Outline each blood parasite and name the species.
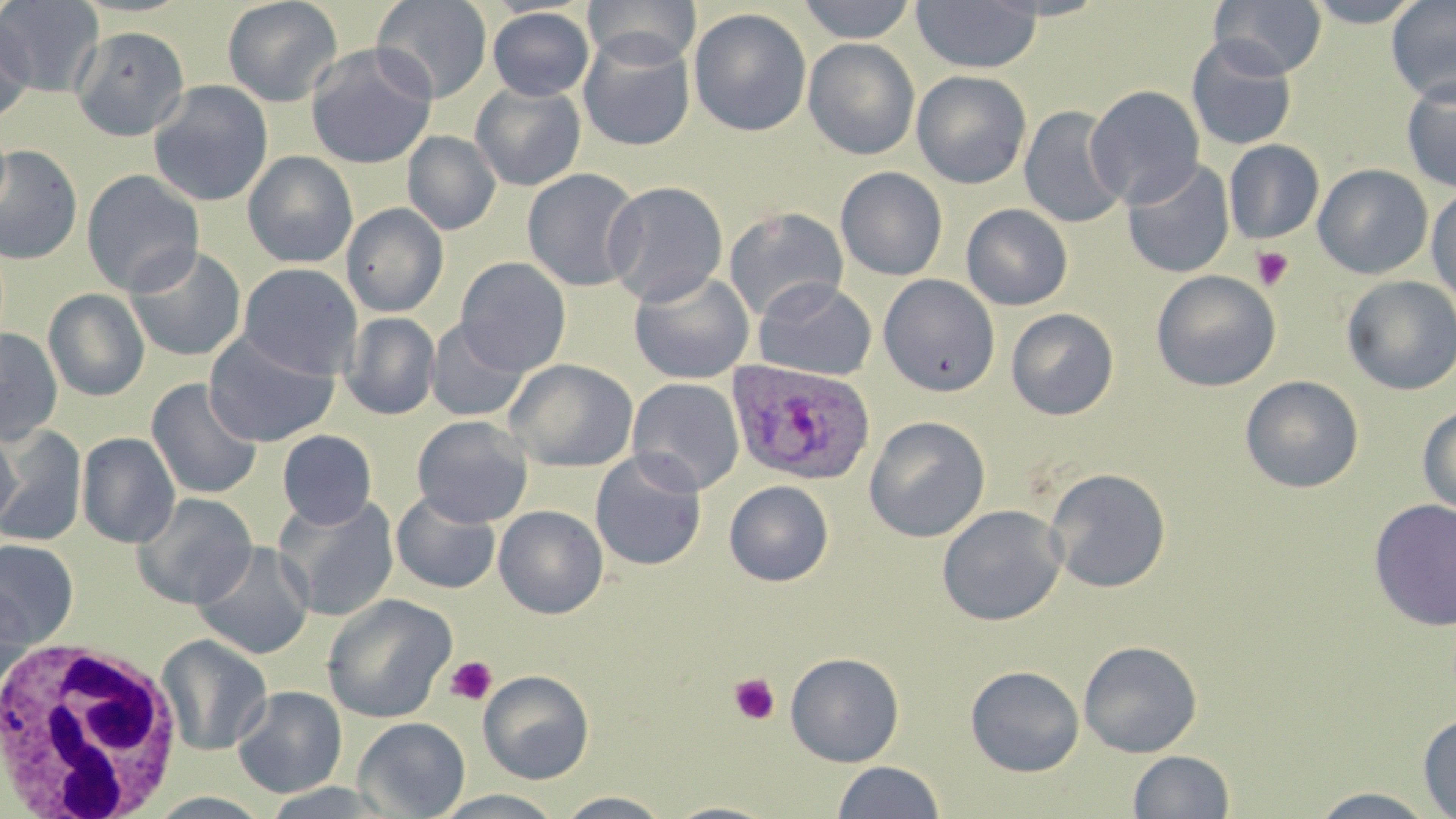

Approximate bounding boxes as [x1, y1, x2, y2] in pixels.
Plasmodium ovale-infected red blood cells: [726, 358, 876, 486].
No Plasmodium falciparum, Plasmodium malariae, Plasmodium vivax, Babesia divergens, or Trypanosoma brucei observed.

{
  "slide_level_diagnosis": "Plasmodium ovale",
  "platelet_locations": "approximate bounding boxes as [x1, y1, x2, y2] in pixels: [1251, 246, 1294, 291], [444, 656, 498, 706], [729, 673, 781, 725]",
  "uninfected_red_blood_cell_locations": "approximate bounding boxes as [x1, y1, x2, y2] in pixels: [0, 0, 105, 97], [222, 0, 343, 107], [371, 0, 493, 104], [583, 0, 701, 68], [796, 0, 918, 43], [911, 0, 1041, 74], [1212, 0, 1327, 79], [1302, 0, 1426, 27], [1387, 0, 1456, 103], [487, 7, 594, 101], [688, 8, 812, 137], [0, 15, 36, 124], [70, 25, 190, 141], [578, 32, 696, 151], [1186, 36, 1298, 152], [803, 38, 919, 159], [305, 44, 437, 169], [911, 70, 1032, 189], [1401, 75, 1456, 194], [147, 80, 274, 207], [470, 82, 586, 192], [1085, 85, 1205, 207], [1019, 105, 1128, 229], [403, 131, 501, 235], [1223, 139, 1323, 244], [0, 144, 83, 265], [243, 151, 358, 268], [1121, 158, 1235, 278], [1313, 164, 1433, 279], [835, 166, 948, 281], [521, 167, 644, 292], [81, 169, 205, 297], [602, 181, 728, 307], [1426, 185, 1456, 307], [341, 203, 449, 317], [961, 203, 1072, 311], [723, 206, 848, 322], [125, 245, 247, 362], [455, 257, 571, 376], [239, 263, 363, 380], [628, 269, 755, 384], [1151, 270, 1281, 391], [878, 274, 1000, 398], [1342, 275, 1456, 395], [752, 278, 877, 381], [43, 288, 150, 401], [1006, 308, 1119, 420], [341, 312, 440, 420], [425, 320, 532, 421], [0, 327, 63, 446], [204, 330, 340, 447], [503, 358, 639, 472], [1241, 375, 1363, 493], [146, 378, 263, 500], [627, 378, 745, 496], [1418, 403, 1456, 516], [412, 415, 534, 528], [864, 416, 990, 543], [0, 425, 21, 532], [0, 427, 87, 547], [277, 430, 377, 528], [77, 432, 180, 549], [589, 450, 708, 571], [1045, 468, 1171, 592], [724, 480, 834, 586], [391, 490, 501, 594], [131, 493, 257, 609], [273, 494, 400, 622], [1368, 499, 1456, 632], [937, 504, 1066, 626], [494, 505, 608, 618], [0, 539, 79, 648], [191, 541, 315, 659], [0, 580, 35, 692], [321, 594, 457, 723], [155, 634, 272, 756], [1079, 640, 1202, 758], [785, 652, 904, 766], [965, 665, 1084, 777], [478, 669, 594, 784], [232, 686, 347, 798], [1418, 713, 1456, 818], [353, 717, 470, 819], [1128, 750, 1235, 818], [832, 761, 945, 819], [258, 783, 402, 818], [1308, 788, 1439, 818], [431, 790, 568, 818], [556, 791, 673, 818], [143, 792, 275, 817], [661, 801, 781, 819]",
  "field_of_view": "one of a larger specimen",
  "image_size": "1456×819 pixels",
  "magnification": "1000x",
  "white_blood_cell_locations": "approximate bounding boxes as [x1, y1, x2, y2] in pixels: [3, 636, 189, 816]",
  "preparation": "thin blood smear",
  "stain": "May-Grünwald-Giemsa",
  "modality": "optical microscopy"
}